Locate and identify every blood parasite.
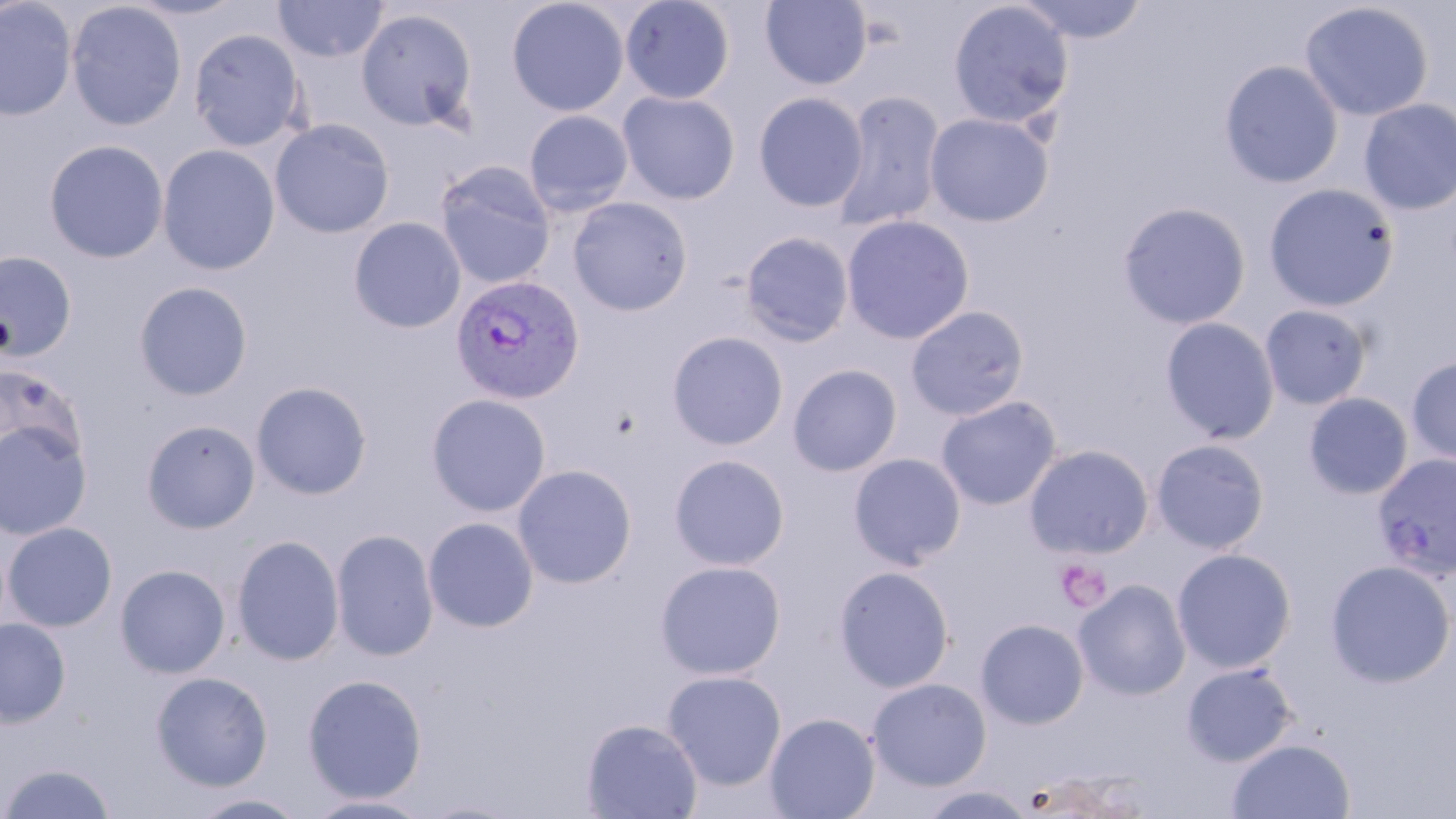

Approximate bounding boxes as (x1,y1)-(x2,y2) corner pairs in pixels.
Plasmodium vivax-infected red blood cells: (450,274)-(585,405).
No Plasmodium falciparum, Plasmodium ovale, Plasmodium malariae, Babesia divergens, or Trypanosoma brucei observed.

Uninfected red blood cell locations: (121,0)-(249,21), (273,0)-(389,62), (506,0)-(629,117), (619,0)-(736,104), (760,0)-(872,90), (1015,0)-(1150,44), (0,1)-(77,121), (65,1)-(187,131), (948,1)-(1075,131), (1298,2)-(1434,121), (355,7)-(479,134), (188,27)-(306,151), (1219,60)-(1343,188), (617,91)-(740,204), (832,91)-(945,232), (753,92)-(868,213), (1358,99)-(1456,215), (523,110)-(633,217), (925,113)-(1054,227), (269,119)-(394,238), (44,139)-(168,263), (157,144)-(280,276), (434,161)-(556,289), (1262,183)-(1399,312), (568,197)-(692,316), (1117,201)-(1252,330), (840,215)-(975,344), (349,217)-(466,333), (740,231)-(855,347), (0,250)-(77,362), (133,281)-(253,400), (1259,304)-(1373,410), (905,305)-(1030,420), (1160,317)-(1280,444), (667,331)-(789,451), (1406,355)-(1456,466), (787,364)-(902,477), (0,365)-(88,467), (250,381)-(373,500), (1303,392)-(1413,500), (426,393)-(551,517), (935,395)-(1062,510), (141,419)-(261,534), (0,420)-(93,540), (1151,438)-(1270,554), (1024,444)-(1154,559), (1372,451)-(1456,580), (848,453)-(966,570), (669,454)-(790,571), (512,464)-(638,589), (423,517)-(539,632), (2,523)-(117,632), (331,529)-(438,662), (231,535)-(344,666), (1172,548)-(1296,673), (1325,559)-(1456,688), (654,560)-(786,680), (115,564)-(231,678), (833,565)-(955,693), (1073,579)-(1192,700), (0,618)-(71,727), (975,618)-(1089,729), (1181,662)-(1298,766), (662,670)-(787,790), (151,671)-(273,791), (302,675)-(427,803), (867,677)-(992,791), (765,712)-(881,819), (581,719)-(703,818), (1226,738)-(1356,819), (1,762)-(117,819), (917,784)-(1040,819), (189,792)-(311,818), (302,794)-(438,818). Platelet locations: (1056,558)-(1112,612). Slide-level diagnosis: Plasmodium vivax. Captured at 1000x magnification. Thin blood film. Optical microscopy. One field of a larger specimen. Image is 1456×819 pixels. May-Grünwald-Giemsa stain.